Locate every malaria parasite.
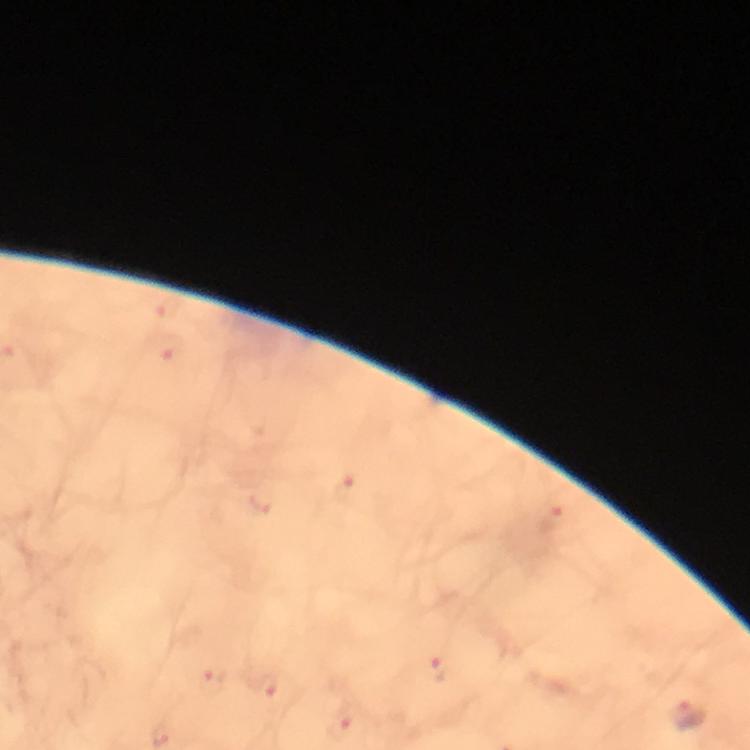
Approximate centers as {x, y} in pixels.
Malaria parasites: {687, 716}.

Summary:
  - Stain: Giemsa
  - Preparation: thick blood film
  - Magnification: 100x
  - Image size: 750×750 pixels
  - Context: from a malaria diagnostic workup
  - Capture: smartphone camera through the microscope
  - Cropped from: one field of view
  - Immersion oil: applied